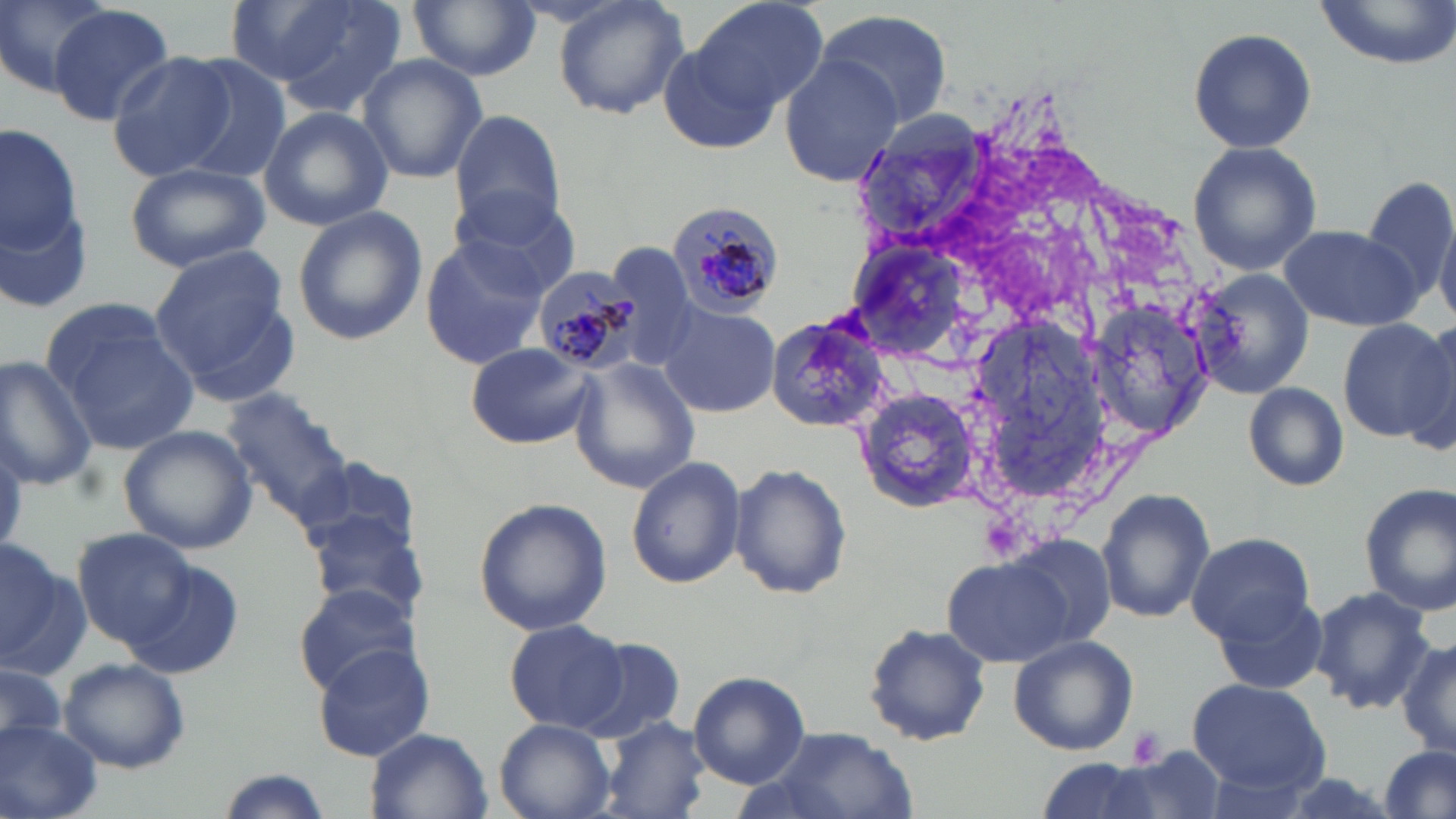 Approximate bounding boxes as (x1,y1)-(x2,y2) corner pairs in pixels. Uninfected red blood cell locations: (1,0)-(118,97), (224,0)-(361,87), (267,0)-(408,119), (409,0)-(541,80), (551,0)-(691,121), (691,0)-(831,115), (1312,0)-(1456,69), (49,5)-(176,126), (812,8)-(954,132), (1186,26)-(1317,154), (654,28)-(787,151), (106,52)-(236,181), (357,54)-(487,182), (779,56)-(900,187), (172,57)-(295,186), (259,104)-(393,229), (450,111)-(568,232), (0,120)-(95,316), (1188,139)-(1323,277), (125,161)-(270,272), (1361,178)-(1456,306), (448,186)-(584,298), (290,204)-(427,347), (1434,216)-(1456,324), (1282,223)-(1424,331), (419,236)-(550,369), (602,243)-(697,369), (150,246)-(298,399), (1191,267)-(1314,397), (44,302)-(199,454), (658,303)-(775,418), (765,310)-(893,433), (1336,317)-(1456,442), (1405,317)-(1456,450), (466,342)-(599,449), (572,355)-(699,496), (0,356)-(98,490), (1243,382)-(1349,491), (855,386)-(981,511), (223,388)-(361,534), (117,425)-(260,554), (297,456)-(420,563), (626,457)-(745,588), (729,462)-(852,599), (1356,483)-(1456,618), (1097,488)-(1215,622), (474,496)-(612,635), (310,511)-(432,625), (74,527)-(195,647), (1186,532)-(1314,644), (0,537)-(84,677), (1010,537)-(1117,651), (943,557)-(1069,666), (120,559)-(245,680), (293,580)-(430,698), (1309,586)-(1435,715), (1212,591)-(1330,695), (504,618)-(631,734), (863,622)-(992,748), (1008,635)-(1139,757), (575,636)-(684,741), (1396,638)-(1456,760), (312,643)-(438,763), (61,657)-(191,774), (0,662)-(65,755), (689,670)-(810,789), (1187,679)-(1327,792), (495,718)-(614,819), (599,718)-(710,819), (0,719)-(102,819), (766,726)-(918,819), (367,728)-(492,819), (1378,746)-(1454,819), (1082,748)-(1227,819), (1034,756)-(1170,819). Plasmodium malariae-infected red blood cell locations: (665,198)-(787,321), (534,265)-(644,374). Platelet locations: (1129,725)-(1169,770). Slide-level diagnosis: Plasmodium malariae. Captured at 1000x magnification. Thin blood smear. One field of a larger specimen. Optical microscopy. May-Grünwald-Giemsa stain. Image is 1456×819 pixels.